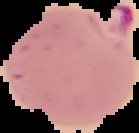

preparation = thin blood smear
image type = cell region segmented out of the field of view; surrounding area masked to black
image size = 139×133 pixels
malaria status = parasitized